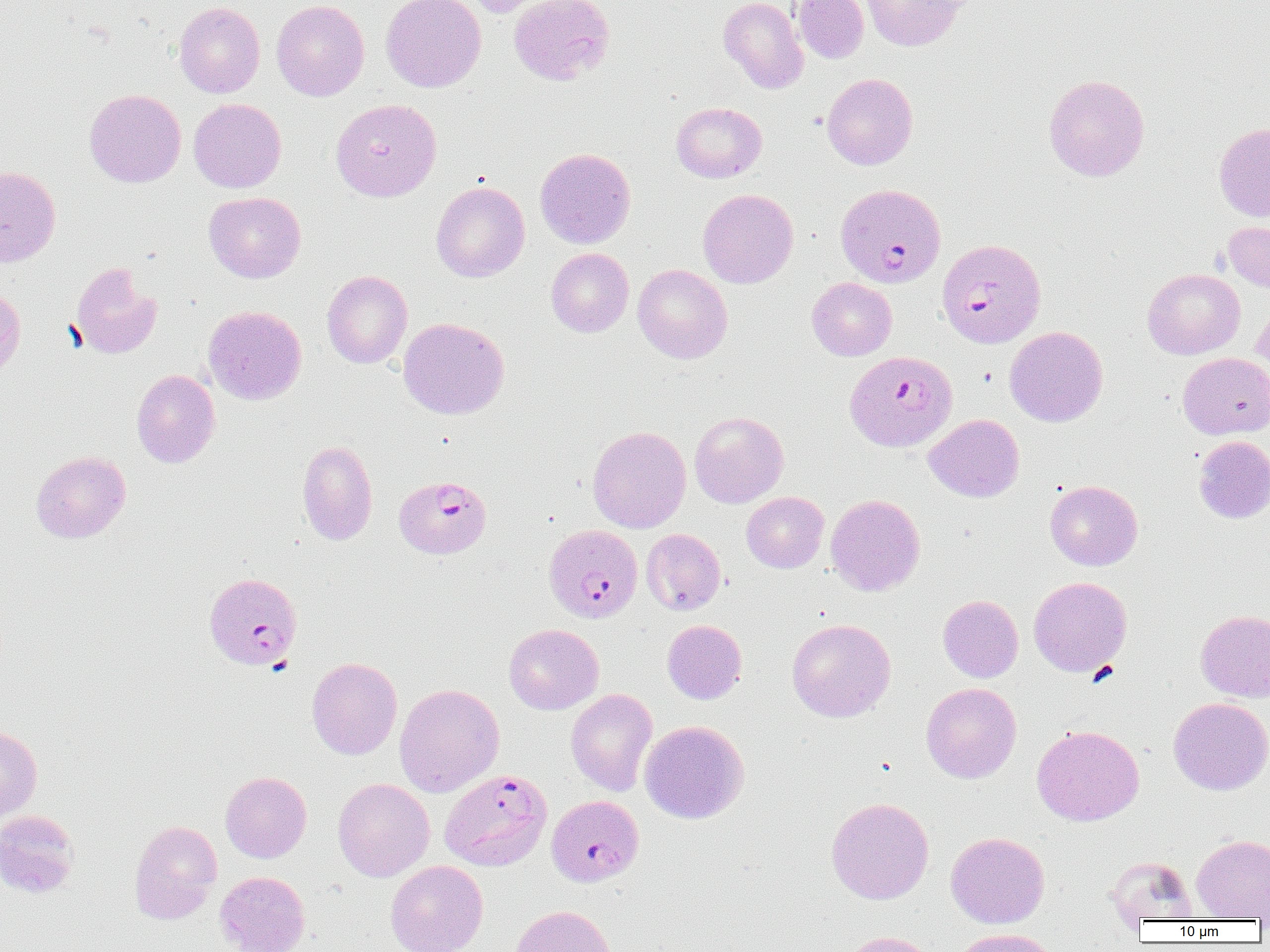

slide-level diagnosis = Plasmodium falciparum
magnification = 1000x
field of view = single
image size = 1270×952 pixels
preparation = thin blood film
uninfected red blood cell locations = approximate bounding boxes as (x1, y1, x2, y2) in pixels: (271, 0, 369, 101), (381, 0, 486, 92), (461, 0, 555, 18), (508, 0, 615, 85), (718, 0, 809, 93), (792, 0, 869, 63), (861, 0, 966, 51), (174, 1, 265, 98), (821, 73, 918, 170), (1043, 74, 1150, 181), (84, 88, 186, 187), (188, 98, 286, 193), (330, 99, 442, 202), (671, 102, 767, 183), (1214, 122, 1270, 222), (535, 147, 636, 249), (0, 166, 60, 267), (431, 181, 530, 282), (697, 188, 798, 288), (203, 192, 306, 283), (1223, 221, 1270, 293), (546, 248, 634, 337), (70, 262, 161, 359), (633, 264, 732, 364), (1142, 268, 1245, 359), (321, 270, 412, 368), (807, 277, 897, 361), (0, 286, 25, 383), (1252, 297, 1270, 379), (203, 305, 307, 405), (398, 317, 509, 419), (1004, 326, 1108, 427), (1178, 352, 1270, 439), (131, 369, 220, 468), (689, 411, 789, 508), (924, 414, 1024, 502), (587, 426, 691, 533), (1194, 435, 1270, 524), (297, 440, 378, 546), (31, 451, 131, 543), (1045, 480, 1143, 570), (741, 492, 829, 573), (825, 494, 925, 596), (641, 528, 725, 615), (1028, 576, 1132, 677), (938, 595, 1023, 682), (1196, 609, 1270, 702), (787, 618, 896, 722), (662, 619, 747, 704), (504, 624, 603, 714), (306, 657, 403, 759), (921, 682, 1021, 783), (394, 683, 504, 797), (566, 688, 658, 797), (1168, 697, 1270, 795), (639, 720, 749, 823), (1032, 724, 1144, 826), (0, 725, 42, 822), (220, 771, 311, 862), (333, 778, 434, 882), (826, 797, 934, 904), (0, 810, 79, 899), (129, 820, 222, 923), (946, 831, 1049, 928), (1191, 834, 1270, 920), (1107, 855, 1196, 924), (386, 861, 488, 952), (215, 871, 310, 952), (508, 904, 615, 952), (952, 928, 1060, 952), (838, 931, 938, 952)
modality = light microscopy
Plasmodium falciparum-infected red blood cell locations = approximate bounding boxes as (x1, y1, x2, y2) in pixels: (836, 184, 946, 287), (936, 238, 1046, 348), (845, 351, 957, 453), (394, 475, 491, 558), (544, 524, 643, 623), (203, 573, 303, 671), (437, 775, 547, 871), (552, 795, 647, 888)